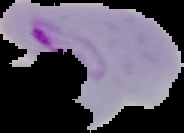
preparation = thin blood smear
image type = segmented cell region on a black background
malaria status = parasitized
image size = 184×133 pixels